Comment on the morphology of the red blood cells.
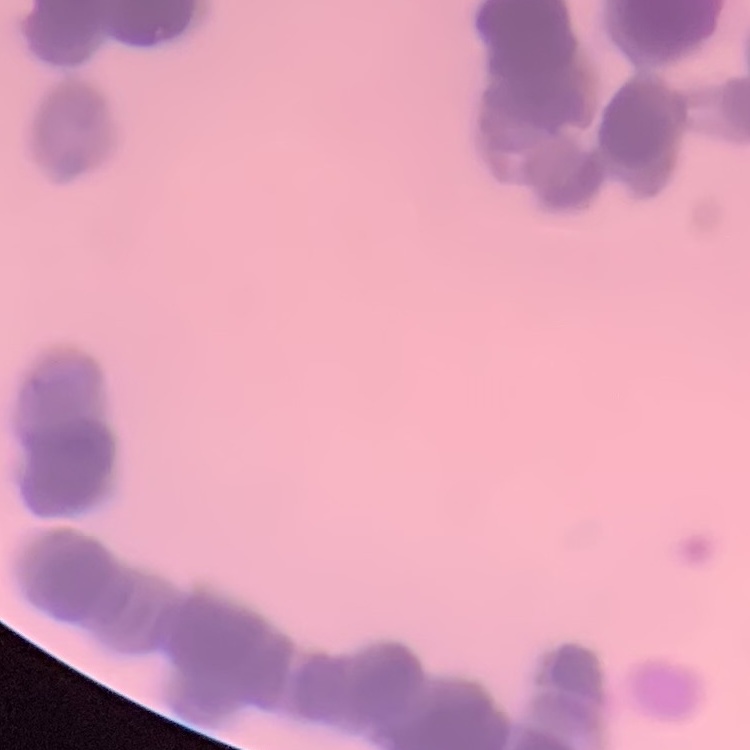
Rouleaux formation.

Summary:
  - Preparation: thin blood smear
  - Stain: Field's or Giemsa
  - Image type: square crop of a larger photomicrograph